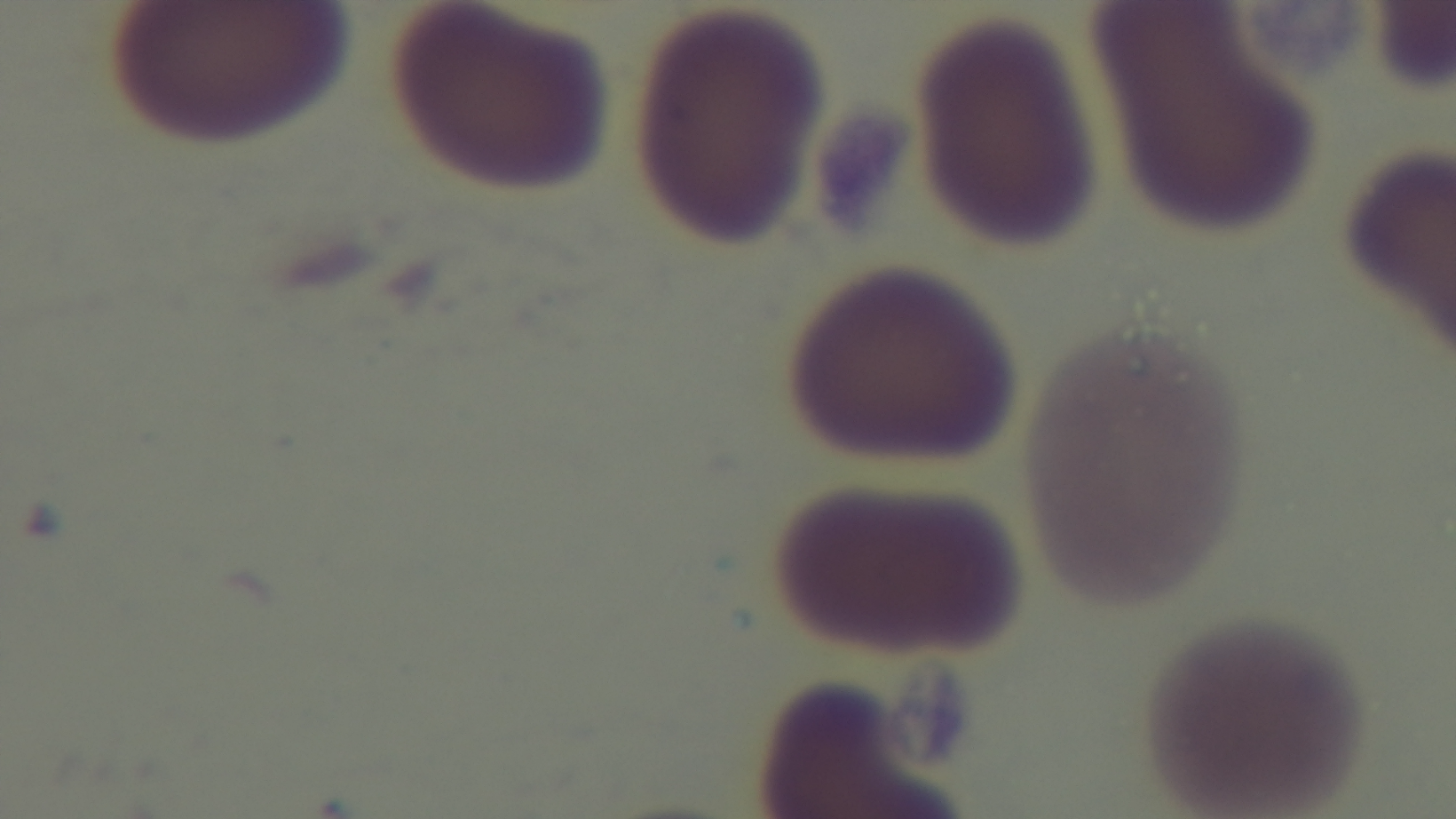
capture: mounted 4K digital camera
objective: 100x oil immersion
stain: Giemsa
modality: light microscopy
field_of_view: one from the slide
preparation: thin blood film
malaria_status: negative